Locate Plasmodium parasites and leukocytes.
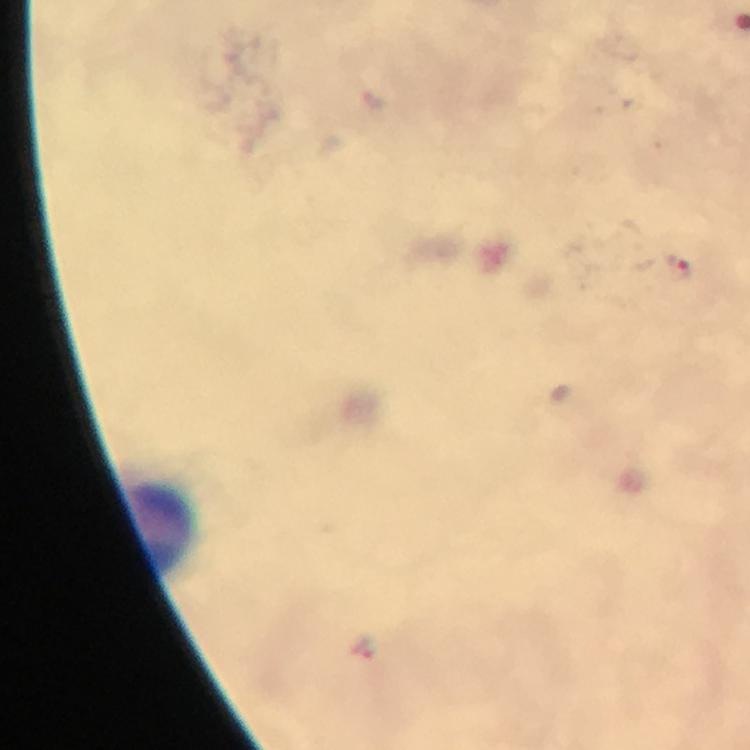
Approximate centers as {x, y} in pixels.
Plasmodium parasites: {677, 268}.
Leukocytes: {154, 523}.

{
  "immersion_oil": "applied",
  "stain": "Giemsa",
  "magnification": "100x",
  "preparation": "thick blood film",
  "context": "from a diagnostic examination for malaria",
  "capture": "smartphone photograph through a microscope",
  "cropped_from": "one field of view",
  "image_size": "750×750 pixels"
}